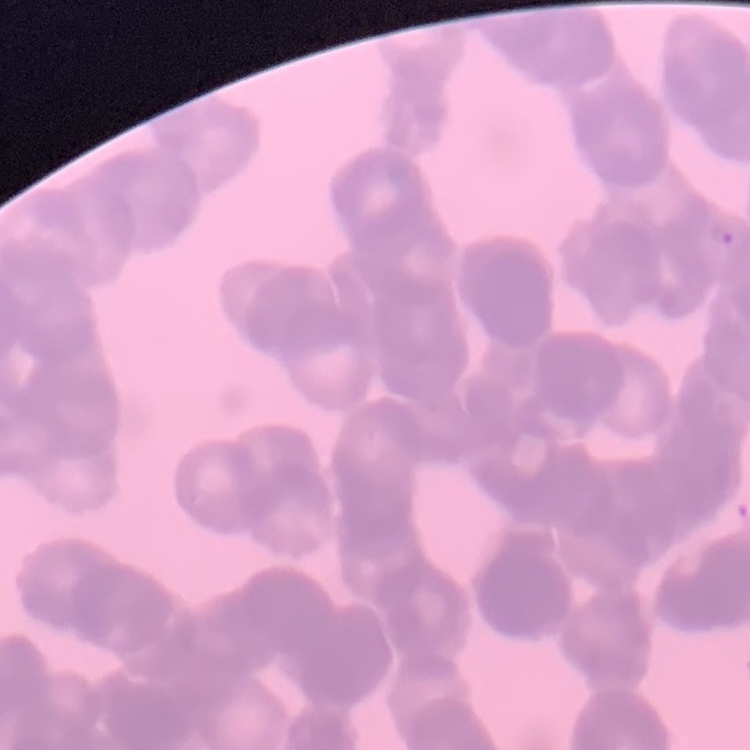
red_blood_cell_morphology: rouleaux formation
preparation: thin peripheral smear
image_type: square crop of a larger photomicrograph
stain: Field's or Giemsa